Locate platelets.
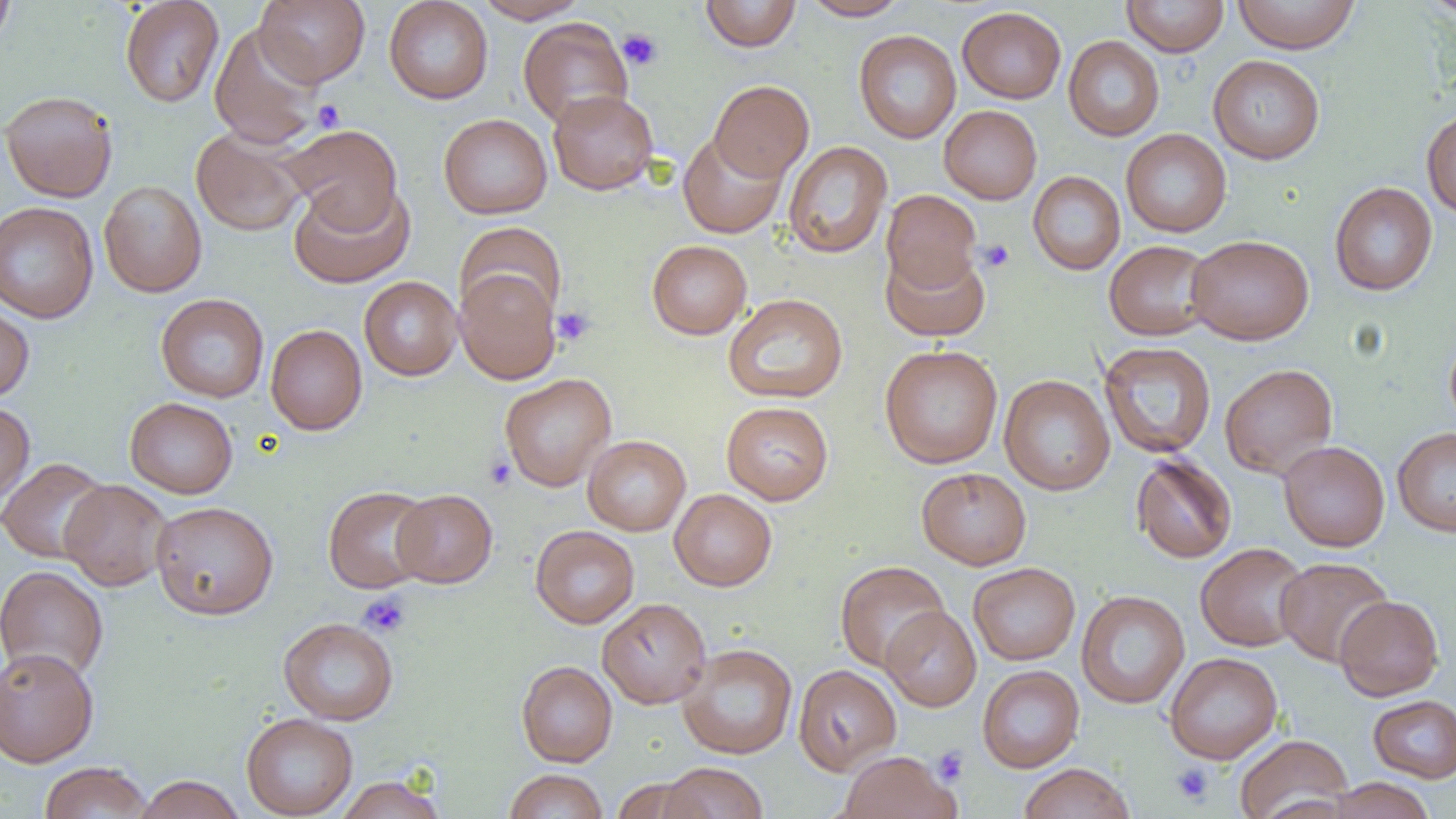
Approximate bounding boxes as (x1,y1)-(x2,y2) corner pairs in pixels.
Platelets: (618,28)-(663,70), (313,100)-(345,131), (977,239)-(1015,273), (552,306)-(596,346), (483,455)-(517,491), (358,592)-(411,638), (932,745)-(969,786), (1169,762)-(1215,806).

Uninfected red blood cell locations: (0,0)-(17,51), (120,0)-(224,108), (255,0)-(370,87), (384,0)-(493,104), (474,0)-(590,23), (700,0)-(801,52), (801,0)-(910,21), (1121,0)-(1229,57), (1231,0)-(1362,54), (1420,0)-(1455,22), (957,6)-(1066,104), (518,17)-(633,128), (209,23)-(324,149), (854,30)-(961,143), (1063,36)-(1165,141), (1208,54)-(1325,164), (709,80)-(814,182), (548,89)-(658,195), (0,90)-(118,202), (939,105)-(1042,204), (1421,110)-(1456,218), (439,113)-(553,219), (281,124)-(403,232), (191,127)-(308,237), (1120,129)-(1232,237), (678,132)-(787,238), (783,141)-(893,259), (1028,171)-(1125,275), (99,180)-(208,297), (288,181)-(415,288), (1329,181)-(1438,296), (881,189)-(981,294), (0,193)-(207,307), (0,201)-(99,323), (454,222)-(567,322), (1186,234)-(1314,345), (647,239)-(752,339), (1104,240)-(1216,341), (880,246)-(990,342), (455,268)-(562,385), (359,276)-(463,380), (723,293)-(848,404), (156,294)-(269,402), (0,302)-(34,402), (265,324)-(367,435), (1445,331)-(1456,435), (1099,341)-(1216,458), (880,344)-(1003,468), (1220,363)-(1338,478), (500,373)-(616,491), (999,374)-(1115,495), (124,397)-(238,498), (0,401)-(35,506), (721,401)-(834,505), (1392,427)-(1456,536), (582,435)-(691,536), (1278,441)-(1390,551), (1131,454)-(1237,563), (0,457)-(111,564), (916,467)-(1031,570), (59,480)-(172,591), (323,484)-(435,593), (393,489)-(497,588), (669,489)-(777,591), (151,500)-(278,619), (530,525)-(639,629), (1195,542)-(1310,651), (1275,556)-(1393,666), (835,560)-(950,673), (968,562)-(1080,665), (0,565)-(108,682), (1076,589)-(1189,709), (1334,595)-(1444,701), (597,598)-(711,709), (881,606)-(981,712), (278,617)-(399,725), (677,643)-(798,759), (0,647)-(99,767), (1164,652)-(1283,764), (516,660)-(617,767), (793,664)-(902,775), (977,665)-(1084,772), (1368,694)-(1456,783), (241,712)-(357,818), (1235,734)-(1353,819), (838,751)-(960,819), (39,761)-(152,818), (658,762)-(769,819), (1017,763)-(1136,819), (504,769)-(608,819), (133,775)-(246,819), (335,775)-(446,819), (1324,777)-(1437,819), (608,778)-(709,818). Slide-level diagnosis: negative for blood parasites. Light microscopy. Thin blood film. Captured at 1000x magnification. Image is 1456×819 pixels. Single field of view.